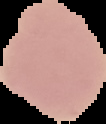
Summary:
  - Result: negative for Plasmodium parasites
  - Preparation: thin blood smear
  - Image type: segmented cell region on a black background
  - Image size: 106×124 pixels